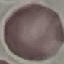

malaria_status: uninfected
stain: Giemsa
image_type: cell patch, automatically extracted from a larger field of view and resized to 64 × 64 pixels
preparation: thin smear
capture: smartphone camera at the microscope eyepiece